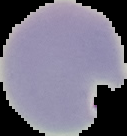
Summary:
  - Image size: 127×136 pixels
  - Malaria status: parasitized
  - Image type: segmented cell region on a black background
  - Preparation: thin blood smear